State which parasite is depicted.
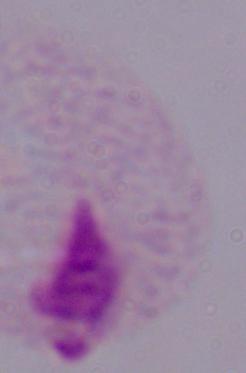

A trichomonad.

Captured at 1000x magnification. Micrograph.